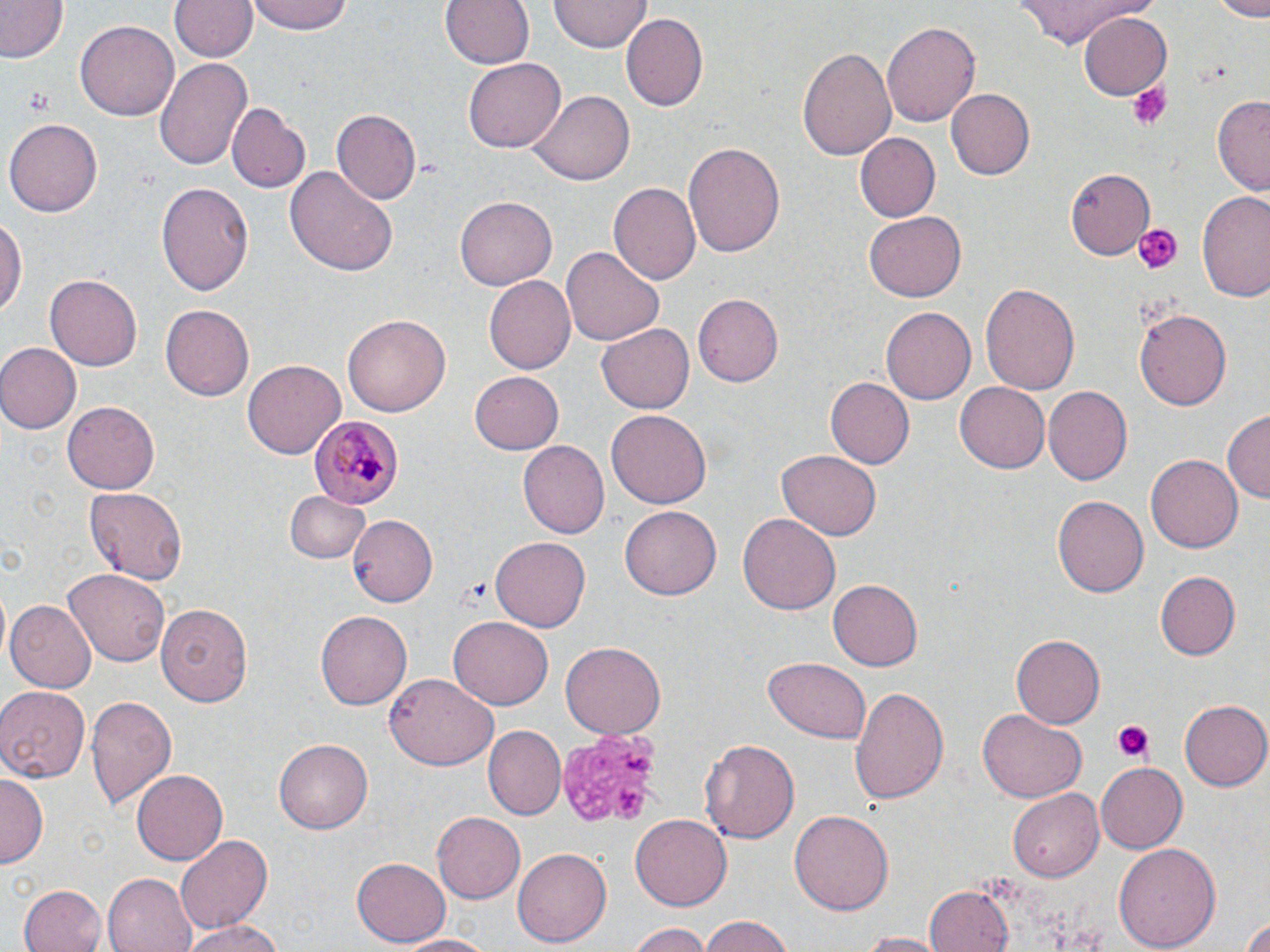

{
  "slide_level_diagnosis": "Plasmodium malariae",
  "platelet_locations": "approximate bounding boxes as (x1, y1, x2, y2) in pixels: (1128, 82, 1174, 132), (24, 91, 52, 112), (1129, 219, 1183, 276), (462, 577, 495, 607), (1113, 722, 1153, 763), (555, 728, 662, 828)",
  "plasmodium_malariae_infected_red_blood_cell_locations": "approximate bounding boxes as (x1, y1, x2, y2) in pixels: (309, 414, 402, 508)",
  "image_size": "1270×952 pixels",
  "stain": "May-Grünwald-Giemsa",
  "modality": "optical microscopy",
  "field_of_view": "single",
  "preparation": "thin blood smear",
  "uninfected_red_blood_cell_locations": "approximate bounding boxes as (x1, y1, x2, y2) in pixels: (0, 0, 68, 66), (166, 0, 260, 64), (250, 0, 352, 35), (441, 0, 534, 70), (548, 0, 648, 52), (1009, 0, 1158, 48), (1211, 0, 1270, 18), (1077, 12, 1171, 101), (621, 15, 707, 111), (76, 18, 181, 119), (881, 20, 979, 129), (800, 44, 897, 164), (154, 58, 251, 171), (464, 58, 564, 153), (946, 88, 1035, 180), (531, 91, 632, 184), (1211, 95, 1270, 196), (228, 102, 309, 193), (330, 109, 421, 206), (6, 118, 103, 216), (854, 132, 939, 222), (684, 139, 784, 260), (286, 165, 397, 278), (1065, 167, 1154, 258), (156, 181, 253, 296), (611, 181, 701, 287), (1198, 192, 1270, 302), (454, 197, 557, 290), (865, 212, 965, 301), (0, 213, 25, 319), (562, 246, 663, 347), (45, 271, 145, 370), (485, 275, 576, 375), (980, 281, 1080, 397), (691, 293, 783, 387), (161, 305, 255, 401), (881, 306, 976, 406), (1135, 307, 1231, 412), (343, 313, 452, 417), (597, 324, 695, 412), (0, 342, 81, 435), (243, 360, 344, 460), (470, 370, 565, 455), (824, 377, 914, 469), (955, 383, 1049, 472), (1043, 387, 1131, 487), (63, 402, 160, 494), (607, 407, 709, 505), (1223, 410, 1269, 504), (517, 441, 609, 539), (776, 451, 882, 541), (1148, 454, 1242, 554), (85, 485, 187, 584), (285, 490, 369, 565), (1053, 496, 1149, 600), (621, 506, 721, 601), (737, 512, 839, 615), (347, 514, 438, 605), (490, 537, 591, 631), (64, 568, 169, 668), (1154, 570, 1241, 661), (830, 578, 923, 671), (5, 599, 95, 694), (157, 604, 252, 707), (317, 610, 412, 710), (448, 616, 553, 711), (1010, 636, 1103, 728), (560, 643, 665, 739), (764, 658, 873, 743), (385, 674, 498, 771), (848, 684, 947, 806), (0, 685, 91, 781), (86, 696, 177, 812), (1180, 698, 1269, 790), (978, 710, 1086, 802), (485, 725, 566, 818), (275, 738, 373, 833), (701, 738, 800, 844), (1096, 763, 1187, 851), (133, 768, 227, 865), (0, 776, 44, 868), (1008, 789, 1103, 881), (791, 810, 893, 915), (630, 811, 733, 911), (432, 812, 524, 906), (173, 833, 273, 935), (1115, 842, 1221, 950), (514, 846, 611, 947), (352, 857, 451, 945), (102, 874, 196, 952), (19, 884, 109, 952), (926, 886, 1014, 952), (700, 915, 798, 951), (182, 917, 281, 952), (1240, 918, 1269, 952), (625, 921, 713, 952), (856, 931, 948, 951), (395, 932, 495, 950)",
  "magnification": "1000x"
}